Identify the blood parasite species.
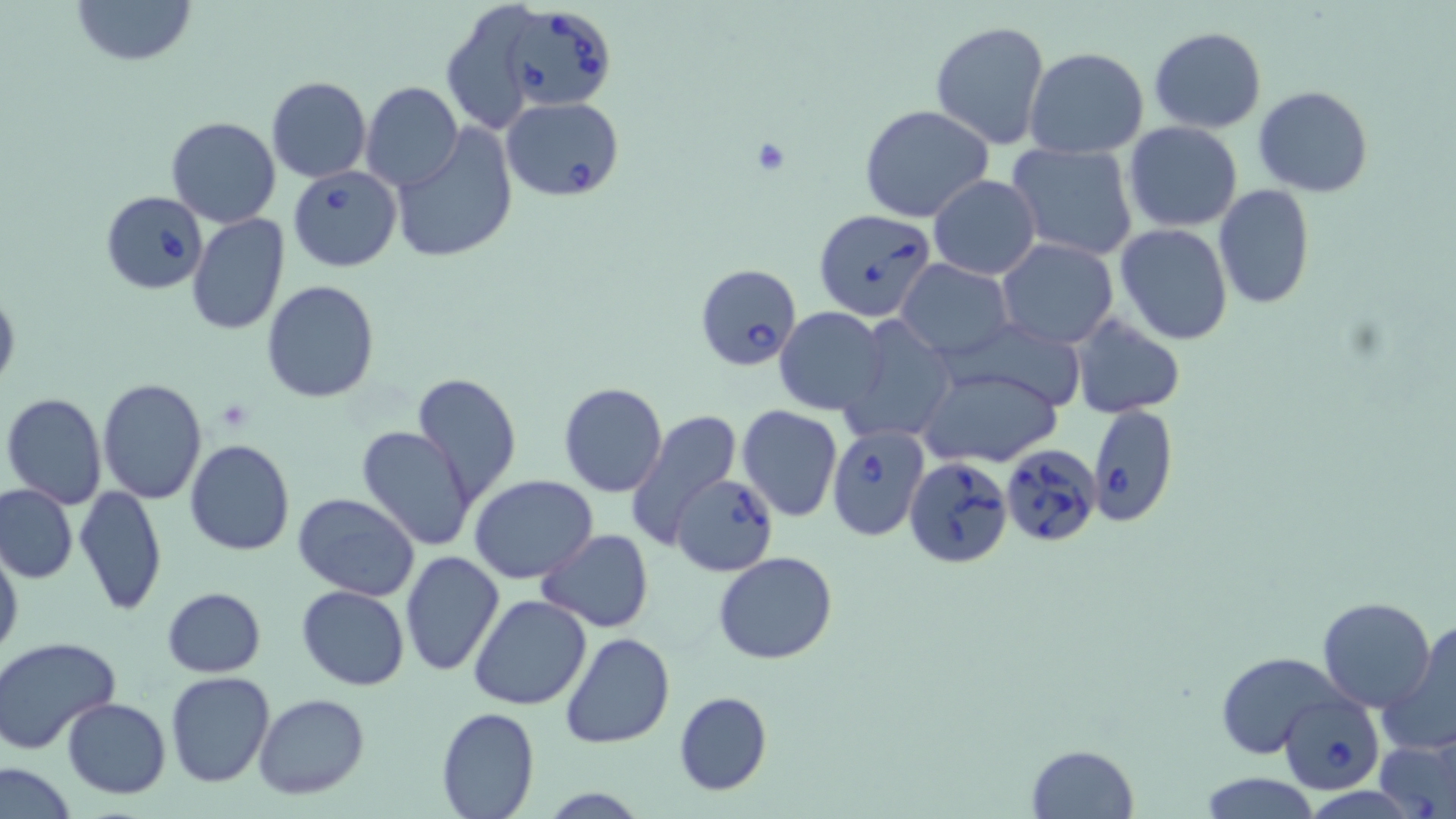
Babesia divergens.

Approximate bounding boxes as (x1,y1)-(x2,y2) corner pairs in pixels. Platelet locations: (752,138)-(792,175). Babesia divergens-infected red blood cell locations: (503,5)-(618,114), (502,97)-(624,202), (288,164)-(401,272), (100,190)-(208,295), (817,209)-(935,318), (694,263)-(802,371), (1086,403)-(1178,528), (826,424)-(929,540), (1000,443)-(1102,550), (904,456)-(1013,568), (670,473)-(779,576), (1279,694)-(1384,794). Uninfected red blood cell locations: (69,0)-(198,68), (440,2)-(550,132), (930,20)-(1052,151), (1149,26)-(1267,132), (1024,48)-(1150,161), (266,76)-(371,184), (360,82)-(462,192), (1255,85)-(1372,197), (860,104)-(994,222), (166,116)-(281,228), (1124,122)-(1244,233), (390,124)-(519,265), (1006,142)-(1139,263), (928,175)-(1042,278), (1213,185)-(1314,311), (187,213)-(292,335), (1114,224)-(1233,346), (995,238)-(1118,349), (896,259)-(1014,362), (262,281)-(380,403), (0,284)-(20,396), (775,307)-(886,414), (1070,315)-(1186,418), (840,316)-(956,444), (948,323)-(1094,412), (916,363)-(1063,467), (412,372)-(523,506), (98,378)-(207,503), (557,382)-(668,497), (2,392)-(108,509), (736,404)-(842,522), (624,408)-(743,549), (356,425)-(478,550), (185,439)-(295,555), (469,475)-(598,583), (0,484)-(78,583), (75,485)-(167,616), (292,492)-(420,602), (537,529)-(655,631), (0,542)-(23,666), (399,551)-(504,678), (713,552)-(838,664), (296,584)-(411,691), (162,588)-(266,676), (469,593)-(592,710), (1318,596)-(1437,711), (1381,621)-(1456,755), (560,631)-(673,749), (0,637)-(122,755), (1214,651)-(1341,756), (167,672)-(276,788), (672,690)-(772,795), (253,693)-(371,800), (63,697)-(170,798), (435,707)-(539,819), (1376,732)-(1455,819), (1026,744)-(1138,817), (0,758)-(80,818), (1200,773)-(1322,818). One field of a larger specimen. Thin blood smear. May-Grünwald-Giemsa-stained preparation. Optical microscopy. Image is 1456×819 pixels. Captured at 1000x magnification.